Locate every Plasmodium parasite.
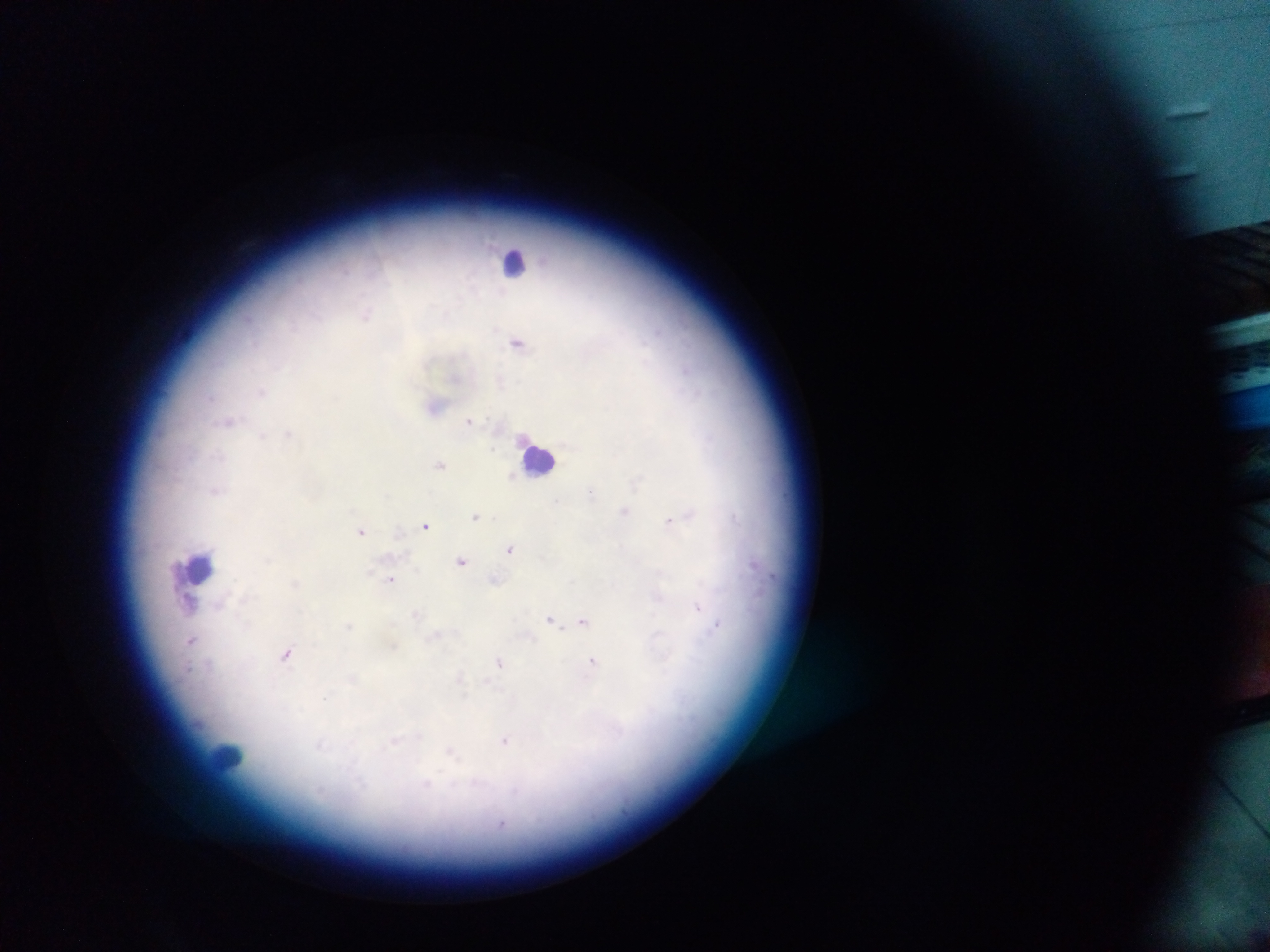
Approximate centers as (x, y) in pixels.
Plasmodium parasites: (366, 315), (518, 342), (685, 369), (261, 391), (209, 398), (469, 420), (230, 421), (288, 435), (262, 436), (441, 464), (512, 476), (636, 481), (216, 491), (591, 492), (556, 501), (625, 512), (689, 514), (476, 516), (669, 521), (426, 526), (361, 531), (510, 549), (268, 560), (461, 561), (390, 579), (494, 580), (295, 583), (656, 597), (189, 603), (221, 604), (698, 608), (416, 614), (551, 619), (583, 621), (348, 626), (715, 627), (435, 636), (191, 641), (394, 646), (286, 655), (499, 662), (592, 664), (188, 669), (459, 678), (353, 679), (325, 697), (395, 741), (506, 741), (320, 744), (451, 753), (426, 784).

preparation: thick blood film
field_of_view: single
country: Ghana
image_size: 1270×952 pixels
leukocyte_locations: 'approximate centers as (x, y) in pixels: (516, 261), (540, 457), (200, 567), (229, 757)'
capture: mobile-phone photograph through a microscope